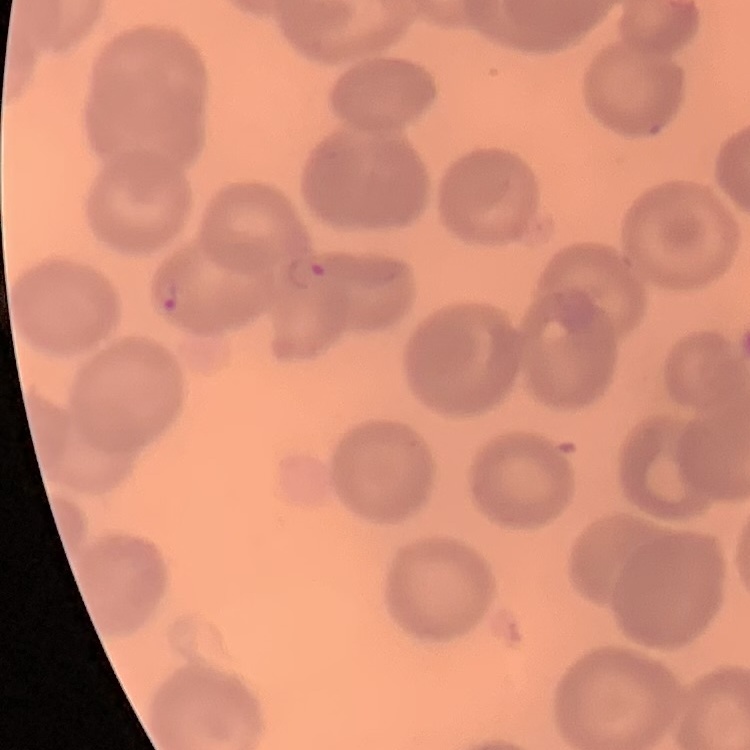
Summary:
  - Red blood cell morphology: no rouleaux formation
  - Stain: Field's or Giemsa
  - Image type: one tile cut from a larger photomicrograph
  - Preparation: thin blood smear